Name the parasite shown.
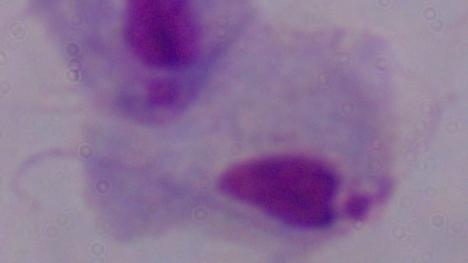
This is a trichomonad.

Summary:
  - Modality: photomicrograph
  - Magnification: 1000x